Locate and identify every blood parasite.
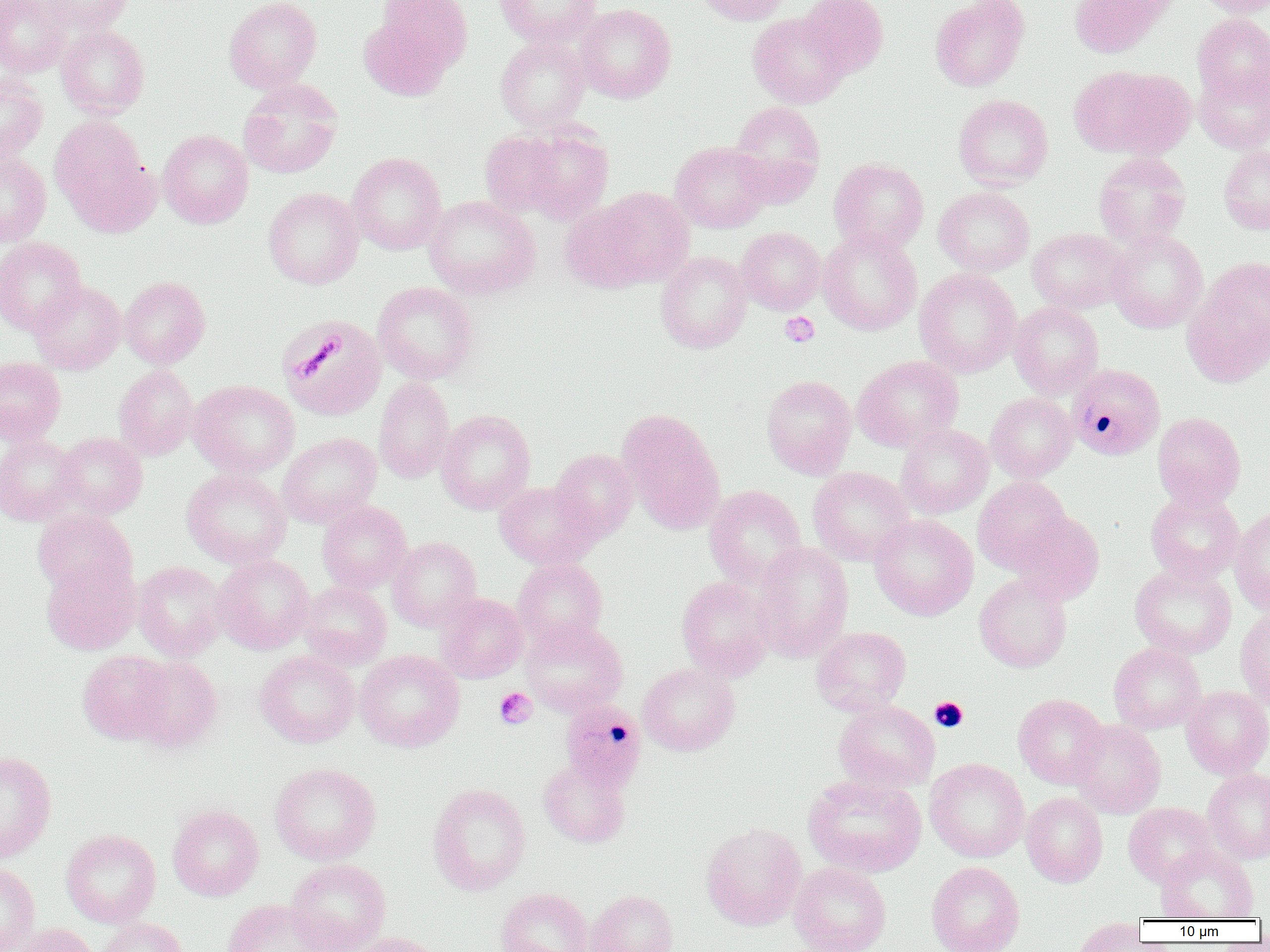

Approximate bounding boxes as (x1, y1, x2, y2) in pixels.
Plasmodium malariae-infected red blood cells: (1067, 363, 1165, 460), (559, 700, 646, 794).
No Plasmodium falciparum, Plasmodium ovale, Plasmodium vivax, Babesia divergens, or Trypanosoma brucei observed.

Summary:
  - Uninfected red blood cell locations: (0, 0, 71, 77), (39, 0, 132, 34), (224, 0, 322, 93), (375, 0, 473, 71), (494, 0, 600, 47), (691, 0, 790, 25), (799, 0, 889, 78), (930, 0, 1029, 91), (1069, 0, 1166, 58), (1196, 0, 1269, 17), (574, 4, 676, 103), (748, 12, 850, 108), (358, 13, 456, 100), (1192, 14, 1270, 106), (56, 25, 150, 118), (495, 35, 591, 132), (1070, 65, 1193, 160), (1194, 65, 1270, 154), (0, 74, 47, 164), (238, 79, 343, 179), (953, 94, 1053, 189), (729, 101, 825, 205), (50, 116, 157, 234), (510, 125, 614, 224), (480, 129, 572, 218), (157, 130, 253, 228), (670, 141, 771, 233), (1218, 144, 1270, 235), (1093, 151, 1191, 249), (347, 152, 446, 255), (0, 153, 51, 246), (829, 158, 928, 254), (584, 186, 695, 288), (934, 186, 1034, 276), (263, 187, 363, 289), (424, 195, 541, 300), (560, 200, 653, 293), (736, 227, 825, 314), (818, 228, 922, 335), (1028, 228, 1130, 314), (1106, 229, 1208, 333), (0, 237, 86, 336), (656, 251, 752, 353), (1203, 256, 1270, 346), (914, 268, 1021, 377), (1182, 273, 1270, 387), (119, 277, 210, 368), (29, 280, 126, 374), (373, 282, 478, 384), (1009, 302, 1104, 398), (277, 315, 386, 421), (852, 356, 963, 451), (0, 357, 66, 443), (113, 364, 199, 460), (761, 374, 856, 479), (374, 377, 455, 483), (189, 380, 299, 477), (985, 393, 1077, 483), (436, 410, 535, 514), (616, 410, 725, 534), (1153, 412, 1246, 509), (895, 424, 993, 518), (55, 432, 147, 518), (277, 433, 381, 527), (0, 434, 81, 525), (551, 449, 638, 541), (808, 467, 914, 566), (182, 468, 291, 568), (973, 476, 1072, 574), (494, 481, 597, 568), (704, 485, 807, 588), (1145, 490, 1243, 583), (317, 501, 412, 593), (1230, 507, 1270, 614), (32, 509, 137, 599), (1010, 511, 1105, 604), (869, 514, 978, 621), (388, 537, 482, 631), (751, 542, 854, 662), (212, 553, 315, 654), (512, 558, 608, 648), (41, 559, 140, 655), (133, 561, 227, 661), (1130, 562, 1237, 659), (974, 573, 1072, 673), (676, 576, 775, 681), (297, 581, 392, 669), (435, 593, 528, 683), (1235, 608, 1270, 711), (521, 620, 627, 717), (811, 626, 911, 716), (1109, 642, 1205, 733), (78, 650, 173, 744), (255, 650, 359, 747), (355, 650, 464, 751), (128, 656, 223, 753), (638, 662, 740, 756), (1182, 686, 1270, 779), (1013, 693, 1108, 789), (833, 698, 939, 793), (1069, 720, 1166, 818), (0, 750, 57, 862), (538, 757, 631, 848), (925, 758, 1029, 862), (269, 762, 381, 865), (1202, 767, 1270, 865), (803, 774, 926, 877), (428, 783, 531, 896), (1021, 792, 1108, 887), (1123, 802, 1218, 887), (168, 804, 264, 901), (701, 822, 806, 930), (61, 829, 161, 927), (1154, 844, 1258, 920), (286, 858, 391, 952), (926, 861, 1025, 952), (0, 862, 40, 952), (788, 862, 891, 952), (495, 888, 594, 952), (587, 889, 678, 952), (223, 899, 336, 952), (97, 918, 188, 952), (1069, 918, 1148, 952), (10, 923, 99, 952), (347, 932, 446, 952)
  - Platelet locations: (780, 312, 819, 347), (295, 335, 344, 379), (494, 687, 537, 729), (929, 697, 968, 732)
  - Slide-level diagnosis: Plasmodium malariae
  - Modality: light microscopy
  - Magnification: 1000x
  - Preparation: thin blood smear
  - Image size: 1270×952 pixels
  - Field of view: single